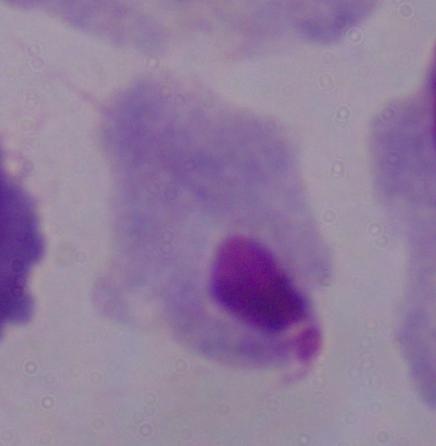

modality = photomicrograph
identification = trichomonad
magnification = 1000x